Give the position of every Plasmodium parasite visible.
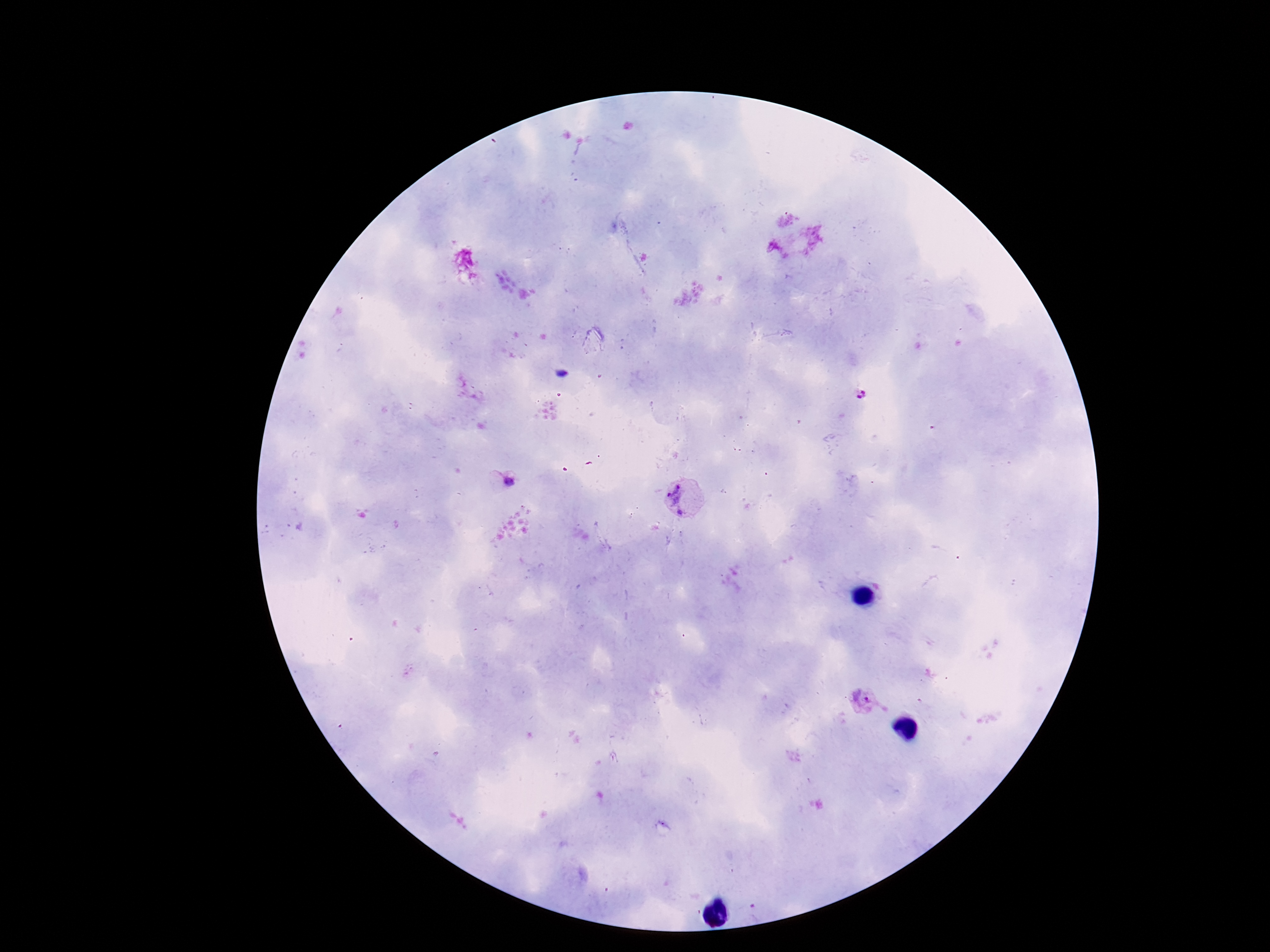

Approximate centers as {x, y} in pixels.
Plasmodium parasites: {861, 394}, {505, 483}, {683, 499}, {864, 703}.

Patient malaria status: positive. Thick peripheral-blood smear. Image is 1270×952 pixels. 100x magnification. Photographed through the microscope eyepiece with a smartphone camera. Giemsa-stained preparation. Single field of view.